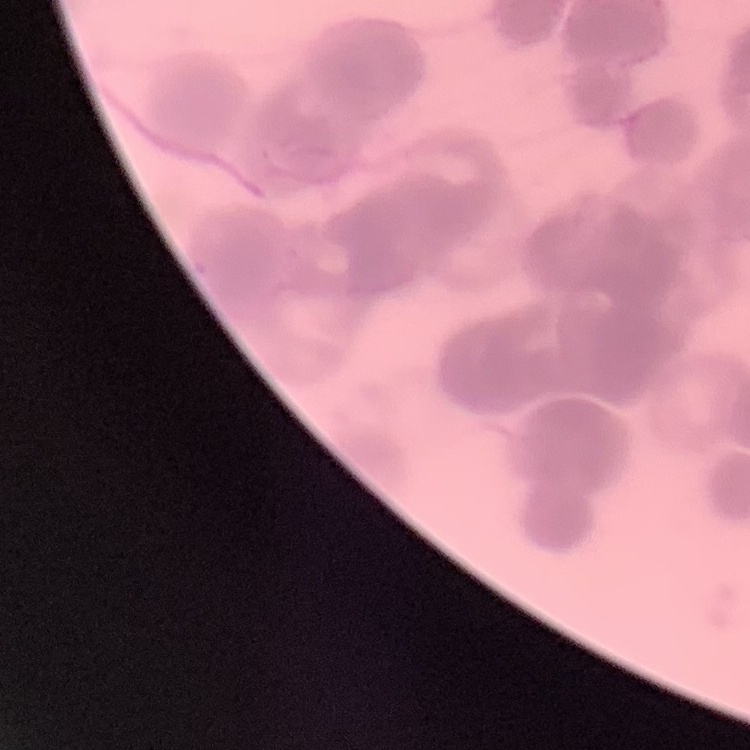
red_blood_cell_morphology: rouleaux formation
preparation: thin blood film
stain: Field's or Giemsa
image_type: square crop of a larger photomicrograph